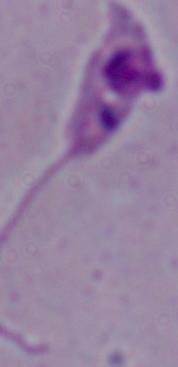

Summary:
  - Modality: micrograph
  - Magnification: 1000x
  - Identification: Leishmania